Name the cell type shown.
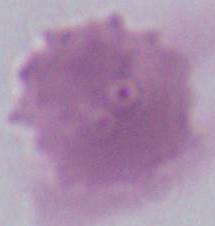

This is an erythrocyte.

magnification = 1000x
modality = photomicrograph